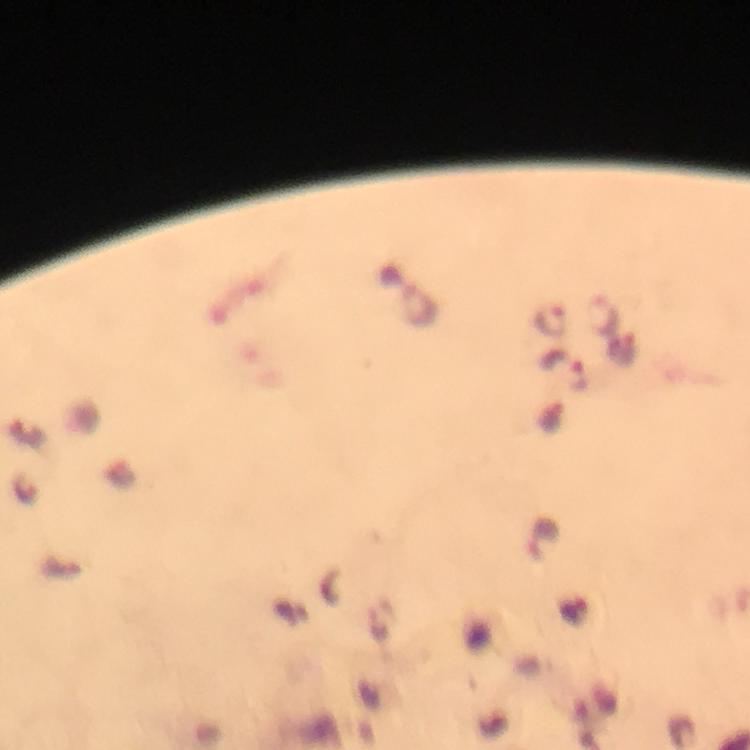

Approximate centers as {x, y} in pixels.
Summary:
  - Malaria parasite locations: {601, 314}, {551, 320}, {622, 352}, {563, 370}, {551, 415}, {25, 487}, {542, 535}
  - Cropped from: a single field of view
  - Stain: Giemsa
  - Magnification: 100x
  - Immersion oil: used
  - Context: from a diagnostic examination for malaria
  - Image size: 750×750 pixels
  - Capture: smartphone camera through the microscope
  - Preparation: thick smear